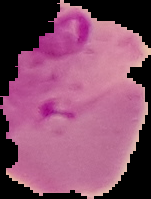
image size = 151×199 pixels
malaria status = parasitized
preparation = thin blood film
image type = segmented cell region with the area outside set to black